Comment on the morphology of the erythrocytes.
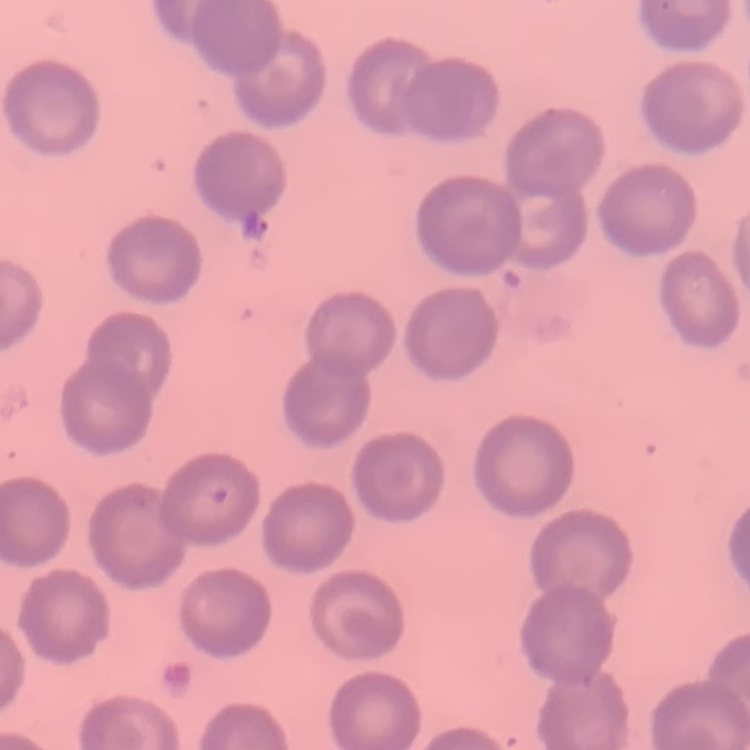

They show no rouleaux formation.

Stained with either Field's or Giemsa. Square crop of a larger photomicrograph. Thin blood smear.